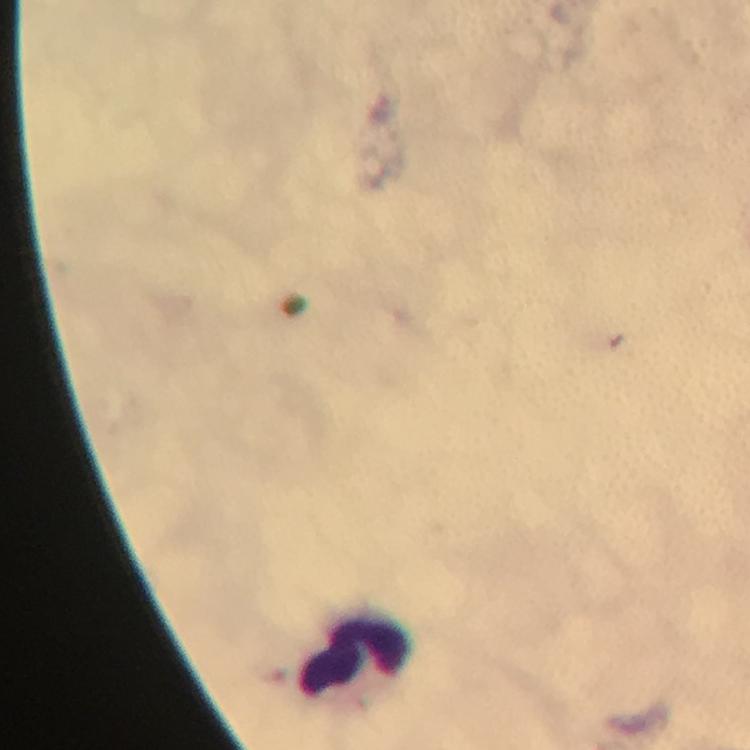
Approximate object centers, in pixels from the top-left corner. Leukocyte locations: (x=357, y=662). Image is 750×750 pixels. Immersion oil was used. Giemsa-stained preparation. Smartphone photograph taken through a microscope. Thick blood film. At 100x magnification. A crop from one field of view. From a malaria diagnostic workup. Plasmodium parasites: none detected.